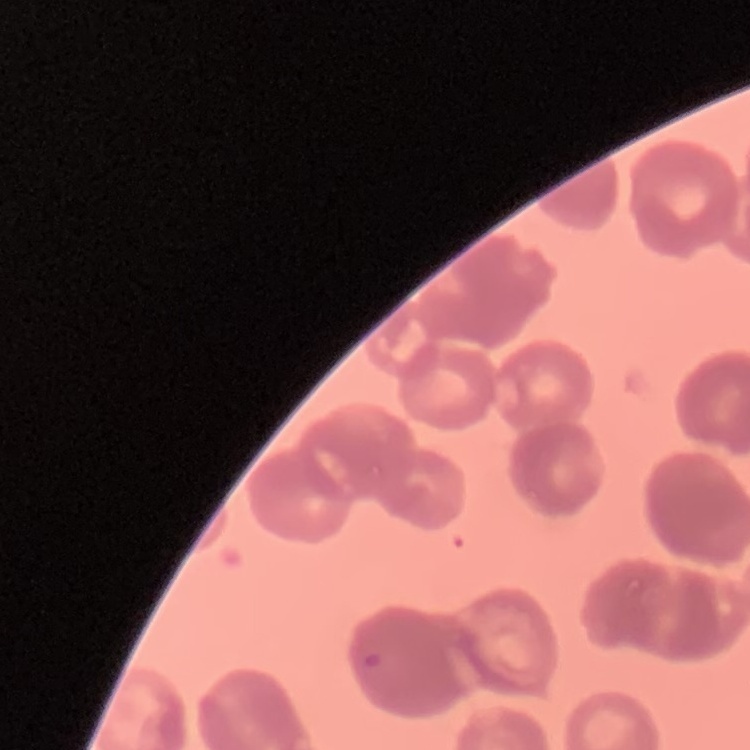

red_blood_cell_morphology: rouleaux formation
stain: Field's or Giemsa
preparation: thin blood film
image_type: one tile cut from a larger photomicrograph